Report the malaria status of this cell.
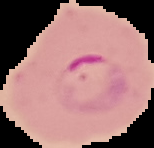
It is parasitized.

Cell region segmented out of the field of view; the surrounding area is masked to black. Image is 154×148 pixels. From a thin blood film.